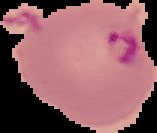 Image is 157×133 pixels. The area outside the segmented cell region is set to black. From a thin blood smear. Malaria status: parasitized.